Assess this cell for malaria.
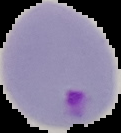

Parasitized.

image size = 121×133 pixels
preparation = thin blood smear
image type = segmented cell region with the area outside set to black